Identify the parasite.
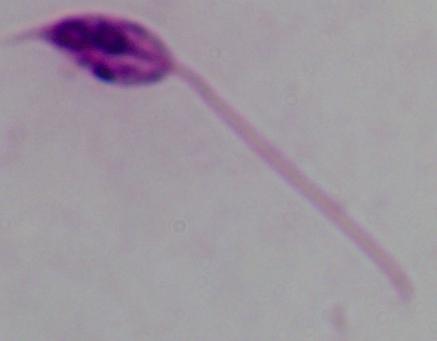

Leishmania.

magnification = 1000x
modality = photomicrograph